Identify the parasite.
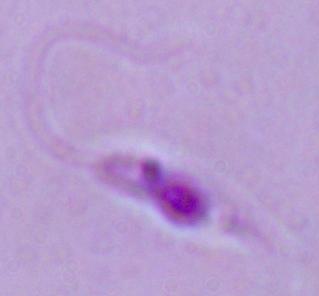
Leishmania.

Summary:
  - Modality: micrograph
  - Magnification: 1000x